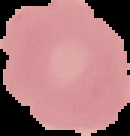

malaria status = uninfected
image size = 130×136 pixels
preparation = thin blood smear
image type = segmented cell region on a black background